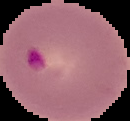

Summary:
  - Malaria status: parasitized
  - Image type: cell region segmented out of the field of view; surrounding area masked to black
  - Preparation: thin blood smear
  - Image size: 130×121 pixels